Assess for malaria.
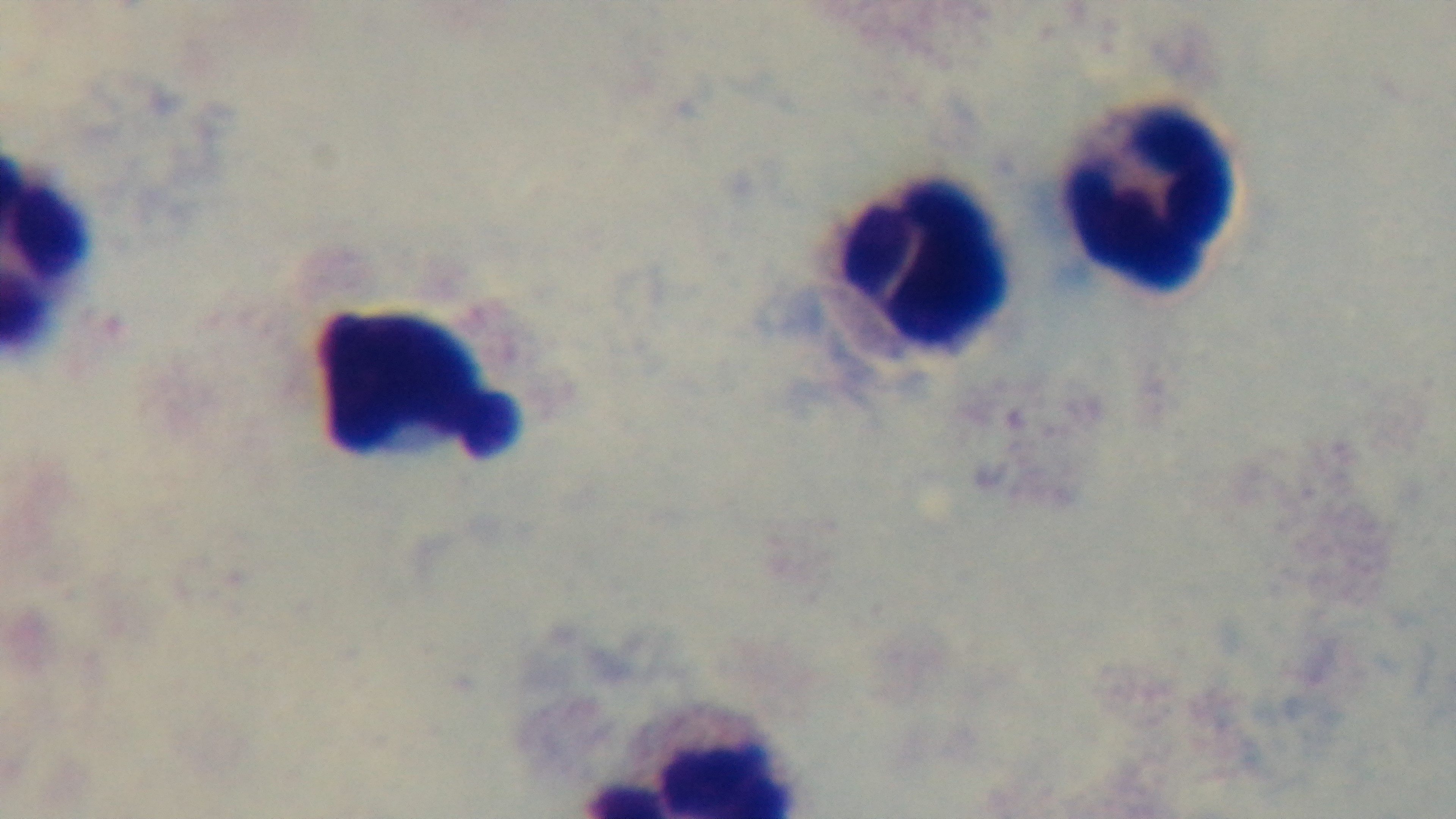

Negative.

Mounted 4K digital camera. 100x oil-immersion objective. Preparation: thick. Giemsa stain. One field from the slide. Photomicrograph.